Name the parasite shown.
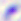
This is Toxoplasma gondii.

{
  "modality": "photomicrograph",
  "magnification": "400x"
}